Locate every malaria parasite.
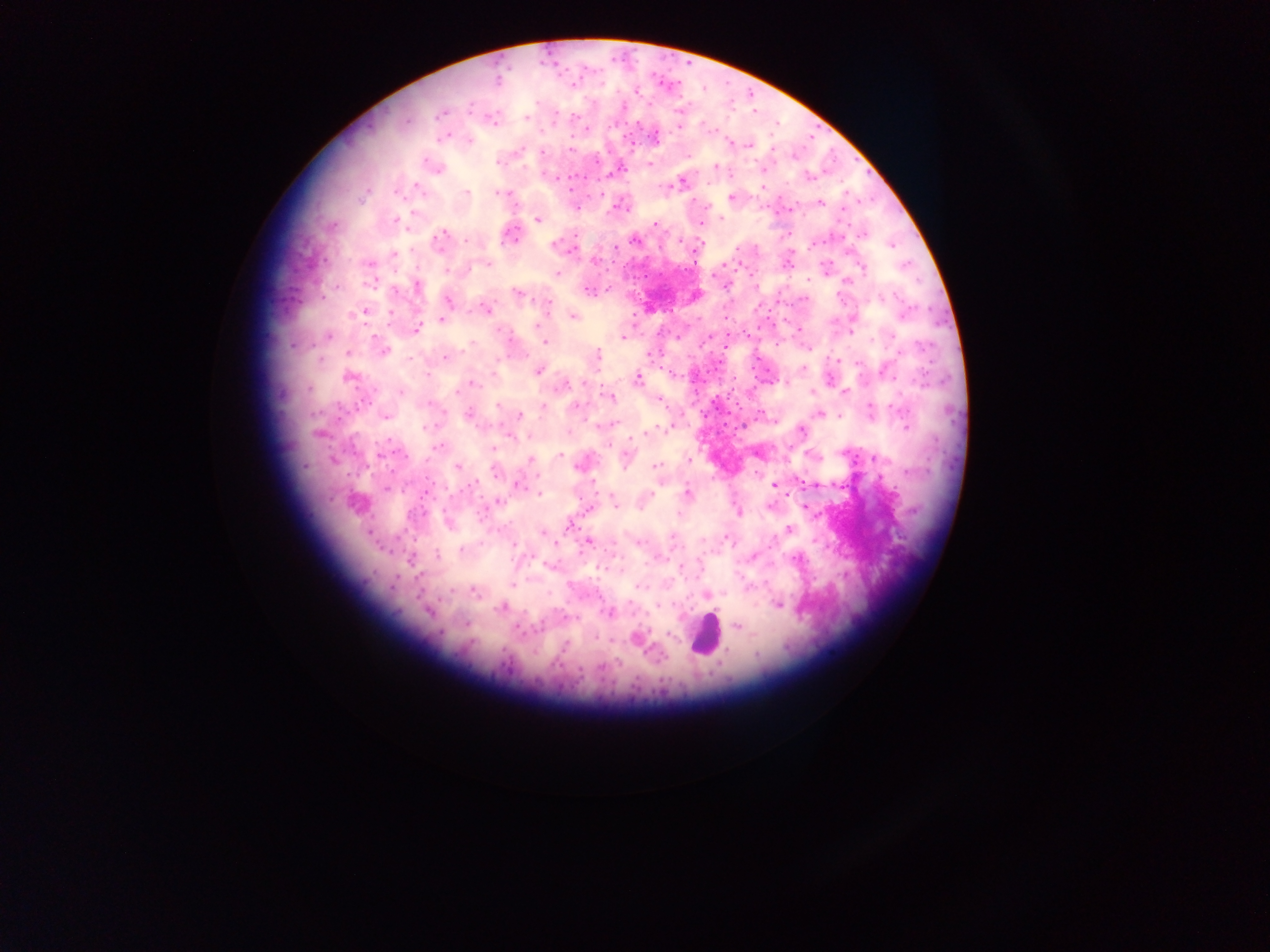
Approximate centers as (x, y) in pixels.
Malaria parasites: (536, 101), (470, 109), (679, 111), (440, 114), (575, 117), (525, 118), (407, 121), (680, 128), (587, 129), (445, 137), (656, 137), (470, 141), (749, 145), (520, 149), (570, 149), (773, 149), (542, 151), (689, 155), (499, 162), (649, 165), (715, 166), (439, 169), (614, 172), (807, 176), (416, 186), (762, 188), (466, 191), (497, 192), (398, 195), (601, 195), (731, 198), (821, 202), (576, 208), (412, 214), (720, 218), (395, 220), (538, 220), (655, 224), (701, 224), (333, 225), (444, 233), (863, 235), (511, 237), (466, 240), (634, 240), (439, 241), (553, 245), (891, 246), (615, 247), (736, 248), (394, 254), (594, 261), (369, 263), (487, 263), (863, 269), (448, 271), (557, 273), (713, 276), (808, 279), (370, 283), (336, 286), (417, 286), (588, 290), (517, 293), (881, 296), (448, 300), (547, 302), (486, 309), (365, 311), (391, 313), (905, 315), (574, 316), (442, 319), (538, 325), (416, 329), (851, 333), (328, 335), (623, 338), (872, 341), (545, 342), (472, 343), (921, 346), (384, 351), (348, 353), (649, 355), (597, 356), (446, 357), (410, 359), (320, 360), (837, 360), (857, 363), (804, 368), (538, 371), (672, 373), (428, 374), (888, 375), (349, 377), (637, 379), (922, 380), (785, 381), (473, 383), (584, 383), (561, 386), (308, 389), (401, 392), (812, 392), (844, 392), (609, 396), (660, 400), (497, 405), (542, 405), (576, 407), (896, 407), (870, 408), (820, 414), (520, 415), (467, 416), (838, 416), (385, 417), (615, 423), (424, 427), (661, 428), (906, 428), (802, 429), (645, 434), (511, 436), (439, 446), (608, 446), (494, 448), (559, 455), (626, 457), (874, 458), (531, 459), (689, 460), (457, 467), (655, 467), (593, 483), (517, 485), (472, 486), (774, 486), (386, 489), (688, 493), (539, 494), (652, 494), (497, 500), (614, 504), (805, 506), (588, 511), (739, 513), (678, 514), (569, 526), (788, 529), (542, 533), (672, 536), (726, 538), (704, 540), (588, 542), (771, 542), (555, 543), (638, 543), (513, 545), (461, 549), (437, 555), (753, 556), (410, 560), (681, 566), (513, 586), (638, 586), (449, 591), (474, 591), (658, 605), (779, 605), (500, 608), (429, 612), (609, 613), (466, 623), (737, 626), (518, 629), (669, 635), (594, 637), (564, 647), (757, 654), (600, 667).

image size = 1270×952 pixels
leukocyte locations = approximate centers as (x, y) in pixels: (705, 634)
preparation = thick blood film
capture = mobile-phone photograph through a microscope
country = Ghana
field of view = single